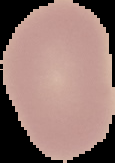
The area outside the segmented cell region is set to black. Image is 115×163 pixels. Result: no Plasmodium parasites seen. From a thin blood film.